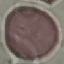
{
  "result": "no malaria parasites seen",
  "image_type": "automatically extracted cell patch, resized to 64 × 64 pixels",
  "stain": "Giemsa",
  "preparation": "thin blood film",
  "capture": "smartphone camera at the microscope eyepiece"
}